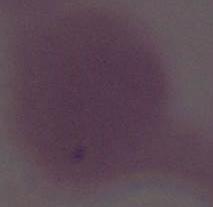
Summary:
  - Identification: red blood cell
  - Modality: photomicrograph
  - Magnification: 1000x